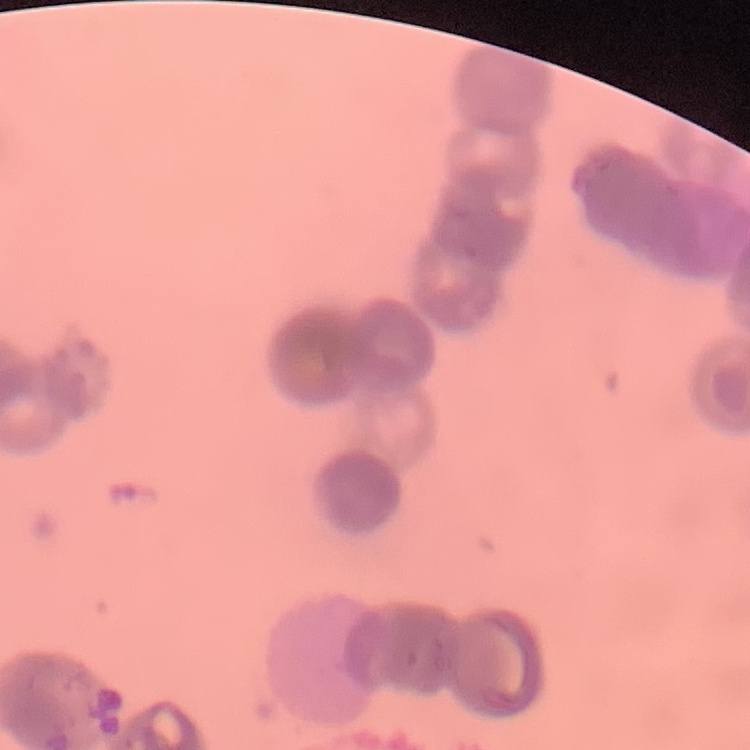
Summary:
  - Red blood cell morphology: rouleaux formation
  - Stain: Field's or Giemsa
  - Image type: one tile cut from a larger photomicrograph
  - Preparation: thin peripheral smear